Rate the background quality.
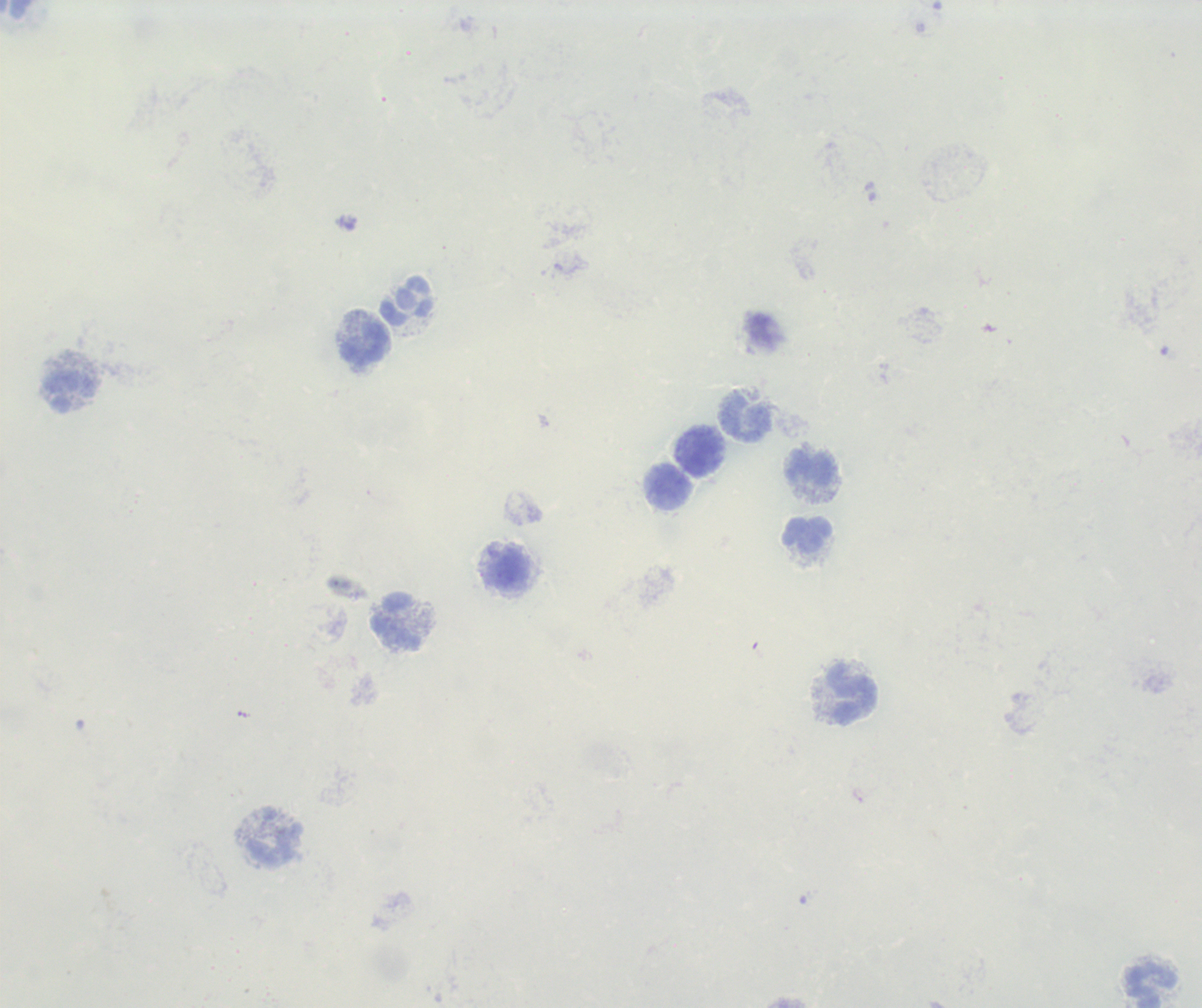

Poor.

{
  "stain": "Romanowsky",
  "image_size": "1202×1008 pixels",
  "leukocyte_locations": "approximate centers as {x, y} in pixels: {16, 10}, {406, 300}, {367, 345}, {71, 391}, {747, 418}, {700, 452}, {812, 469}, {669, 486}, {807, 534}, {509, 571}, {399, 623}, {853, 694}, {273, 845}, {1153, 986}",
  "context": "previously used in an actual diagnosis",
  "preparation": "thick blood film",
  "magnification": "100x",
  "field_of_view": "one from this slide",
  "result": "negative for Plasmodium parasites"
}